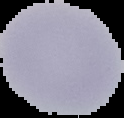 Image is 124×118 pixels. Result: no Plasmodium parasites detected. Cell region segmented out of the field of view; the surrounding area is masked to black. From a thin blood film.